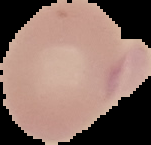 Result: negative for Plasmodium parasites. From a thin blood film. Image is 151×145 pixels. Segmented cell region on a black background.